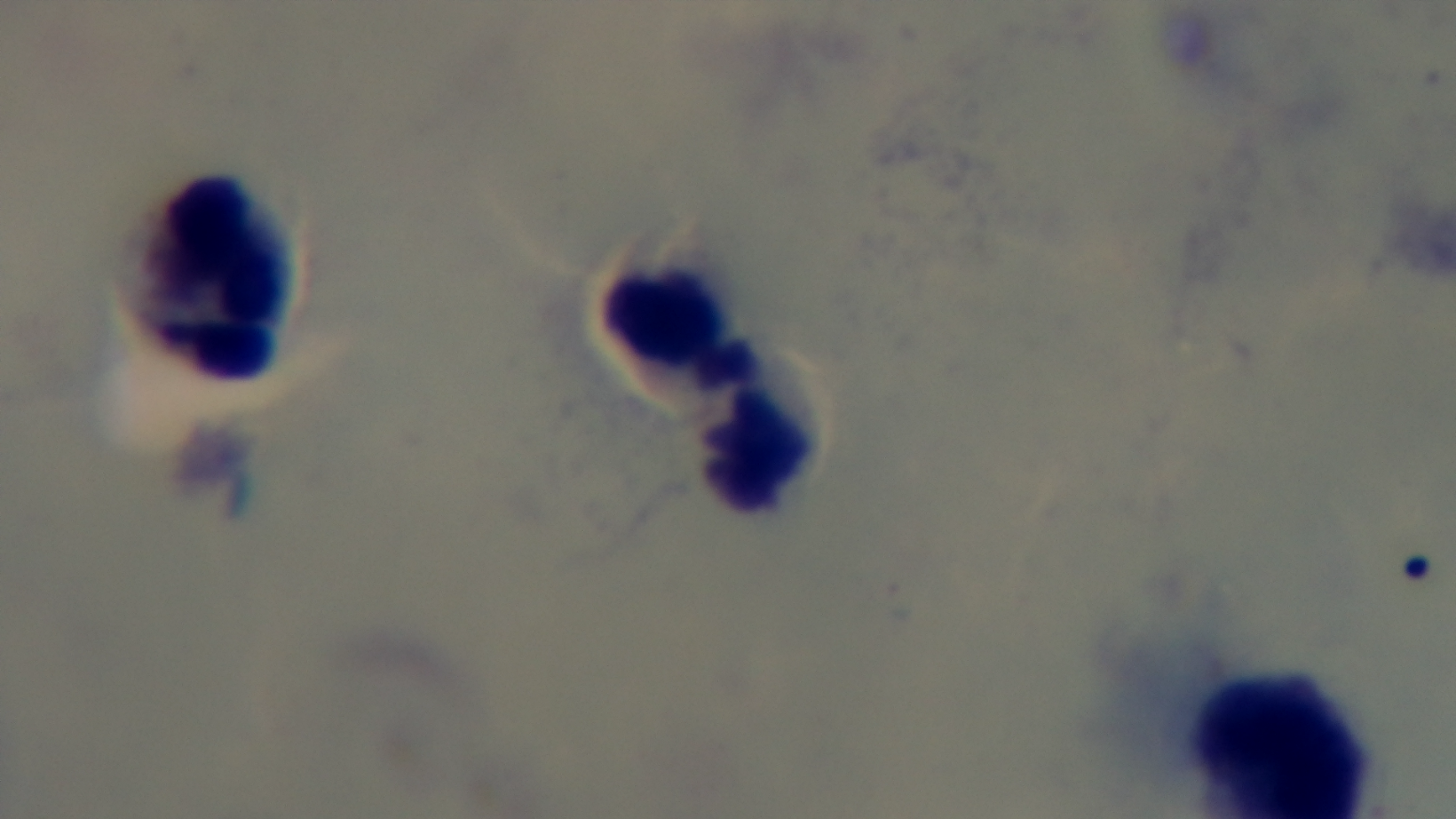
modality = light microscopy
field of view = single
preparation = thick blood film
objective = 100x oil immersion
malaria status = negative
stain = Giemsa
capture = mounted 4K digital camera